Name the parasite shown.
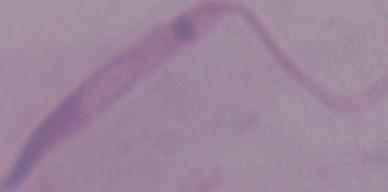

Leishmania.

Micrograph. Captured at 1000x magnification.